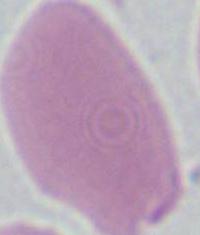

Summary:
  - Identification: red blood cell
  - Magnification: 1000x
  - Modality: micrograph